Mark where leukocytes are.
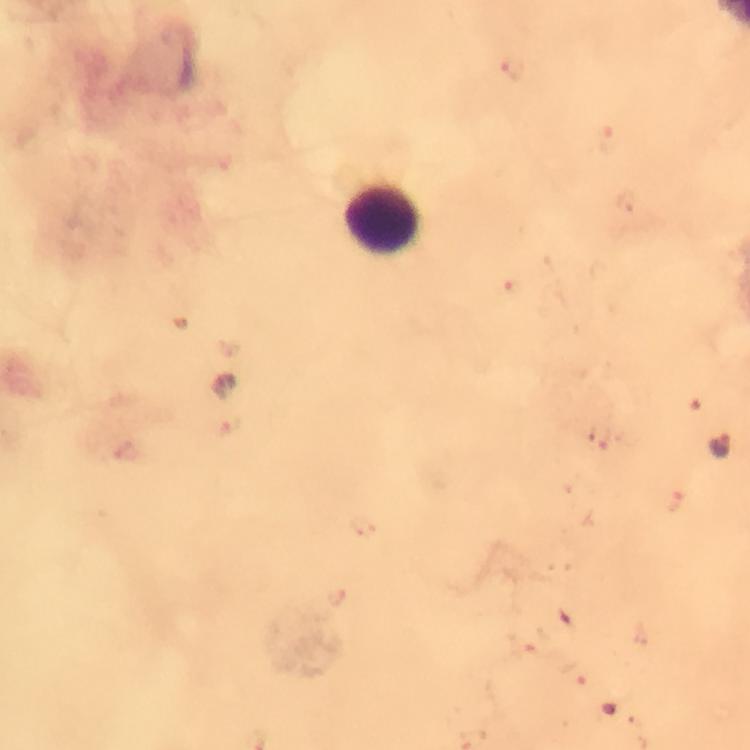
Approximate object centers, in pixels from the top-left corner.
Leukocytes: (x=381, y=218).

context: from a diagnostic examination for malaria
immersion_oil: applied
stain: Giemsa
image_size: 750×750 pixels
plasmodium_parasite_locations: 'approximate object centers, in pixels from the top-left corner: (x=720, y=445)'
cropped_from: a single field of view
capture: smartphone camera through the microscope
magnification: 100x
preparation: thick smear